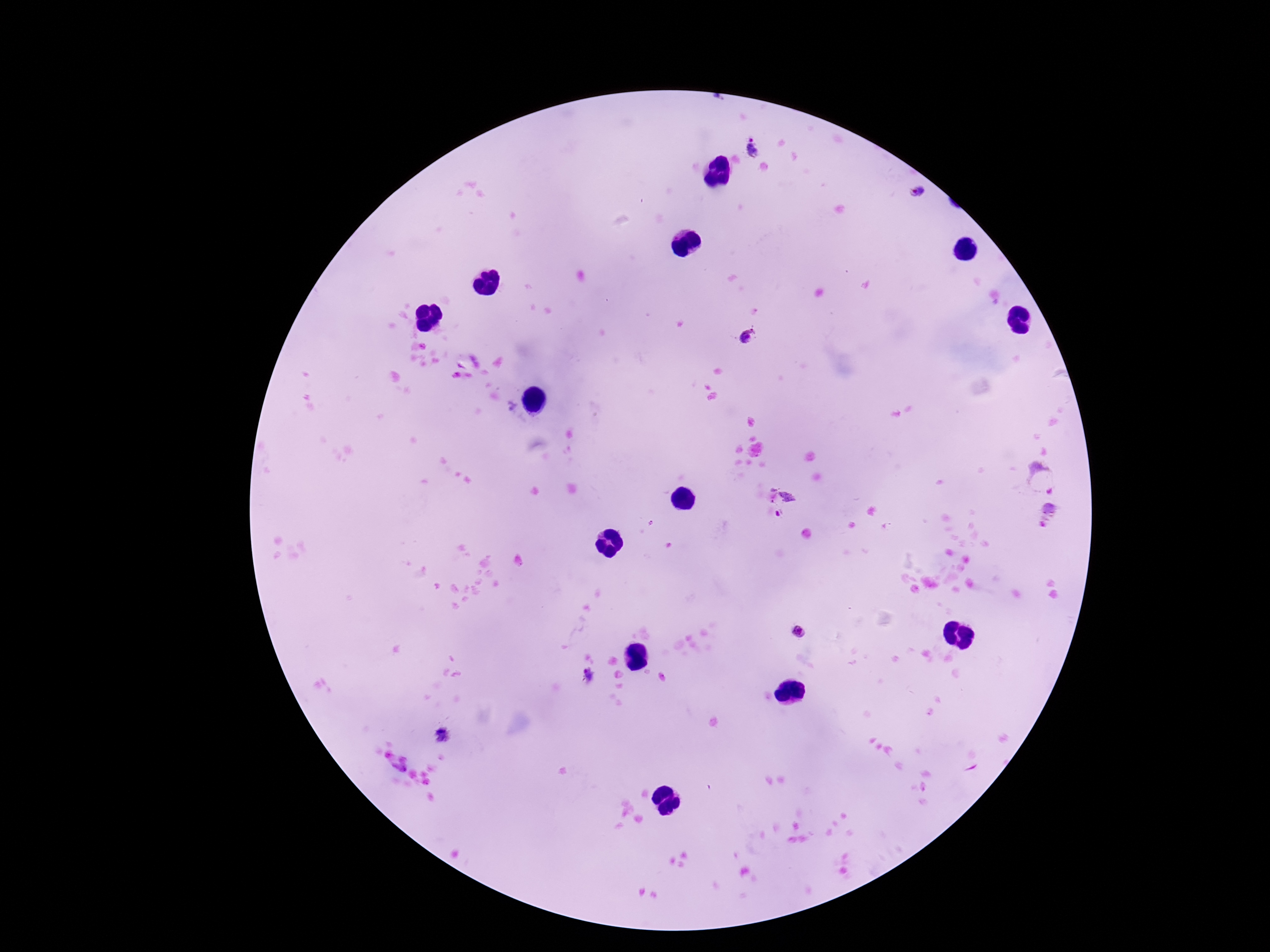
Approximate centers as {x, y} in pixels.
Summary:
  - Plasmodium parasite locations: {750, 145}, {916, 191}, {751, 337}, {1043, 477}, {781, 496}, {777, 514}, {1050, 515}, {799, 632}, {588, 675}
  - Image size: 1270×952 pixels
  - Stain: Giemsa
  - Patient malaria status: positive
  - Field of view: single
  - Magnification: 100x
  - Preparation: thick blood smear
  - Capture: smartphone camera through the microscope eyepiece